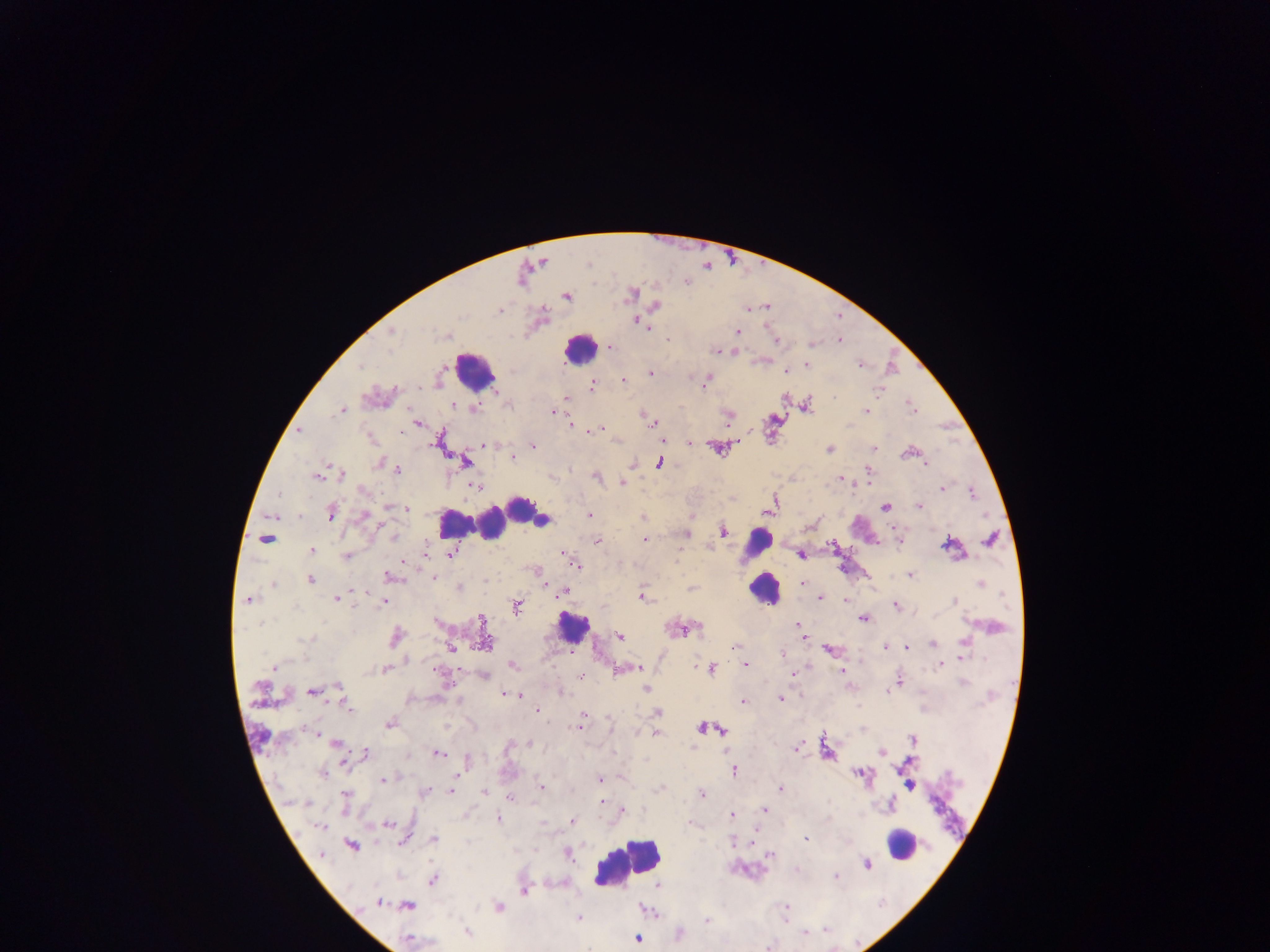

leukocyte_locations: 'approximate centers as {x, y} in pixels: {581, 352}, {480, 368}, {493, 513}, {754, 538}, {759, 597}, {568, 633}, {902, 842}, {630, 863}'
image_size: 1270×952 pixels
preparation: thick blood film
country: Ghana
field_of_view: single
malaria_parasite_locations: 'approximate centers as {x, y} in pixels: {637, 321}, {648, 328}, {736, 331}, {837, 341}, {610, 345}, {812, 347}, {715, 352}, {807, 365}, {860, 365}, {363, 369}, {787, 371}, {651, 373}, {623, 379}, {591, 385}, {702, 387}, {878, 390}, {834, 396}, {566, 398}, {910, 405}, {341, 409}, {409, 409}, {867, 409}, {911, 409}, {551, 411}, {642, 414}, {653, 422}, {730, 422}, {418, 423}, {570, 423}, {421, 426}, {601, 427}, {298, 431}, {589, 432}, {401, 434}, {734, 441}, {688, 443}, {482, 444}, {534, 446}, {829, 449}, {875, 449}, {912, 449}, {908, 453}, {512, 456}, {464, 462}, {925, 465}, {400, 470}, {870, 472}, {342, 473}, {316, 477}, {837, 477}, {597, 478}, {622, 482}, {476, 486}, {940, 487}, {973, 492}, {280, 495}, {919, 505}, {388, 507}, {886, 507}, {408, 510}, {591, 515}, {329, 516}, {642, 517}, {722, 532}, {687, 533}, {392, 534}, {266, 540}, {645, 540}, {595, 541}, {899, 544}, {942, 545}, {311, 549}, {425, 552}, {561, 553}, {450, 554}, {801, 556}, {346, 557}, {678, 557}, {402, 560}, {577, 565}, {910, 575}, {388, 577}, {432, 577}, {310, 580}, {543, 583}, {804, 584}, {272, 585}, {640, 588}, {691, 588}, {355, 591}, {565, 592}, {640, 598}, {820, 599}, {247, 600}, {338, 601}, {845, 601}, {382, 602}, {894, 606}, {354, 607}, {517, 610}, {862, 619}, {480, 621}, {798, 625}, {620, 638}, {804, 640}, {482, 642}, {934, 643}, {735, 645}, {884, 646}, {908, 647}, {449, 648}, {828, 650}, {782, 654}, {963, 656}, {745, 664}, {940, 664}, {512, 666}, {272, 667}, {433, 669}, {638, 669}, {710, 670}, {841, 670}, {620, 671}, {793, 674}, {581, 677}, {962, 681}, {338, 687}, {645, 689}, {310, 693}, {504, 693}, {887, 693}, {519, 695}, {779, 700}, {743, 701}, {346, 706}, {536, 711}, {658, 712}, {583, 716}, {583, 723}, {388, 724}, {579, 726}, {304, 728}, {310, 730}, {320, 734}, {656, 734}, {335, 741}, {796, 749}, {367, 753}, {438, 755}, {643, 758}, {344, 762}, {734, 772}, {322, 774}, {458, 775}, {598, 780}, {384, 781}, {542, 788}, {780, 788}, {449, 790}, {483, 791}, {701, 794}, {345, 796}, {509, 797}, {602, 800}, {602, 804}, {622, 810}, {765, 810}, {731, 816}, {497, 818}, {574, 820}, {320, 828}, {805, 838}, {732, 840}, {403, 841}, {770, 855}, {835, 877}, {433, 881}, {524, 891}, {705, 921}, {825, 932}, {803, 934}'
capture: mobile-phone photograph through a microscope